Describe the morphology of the erythrocytes.
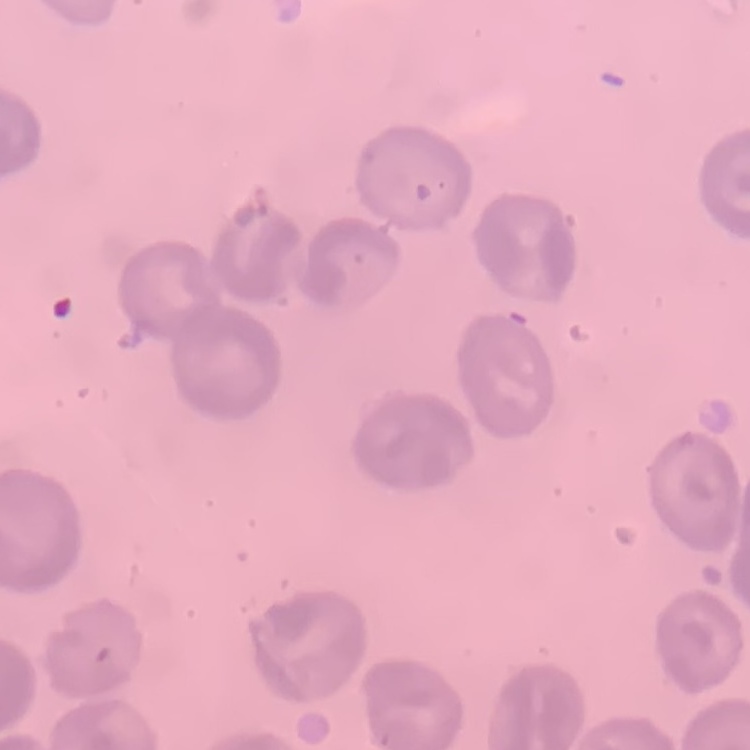

They show no rouleaux formation.

Summary:
  - Preparation: thin blood smear
  - Image type: square crop of a larger photomicrograph
  - Stain: Field's or Giemsa